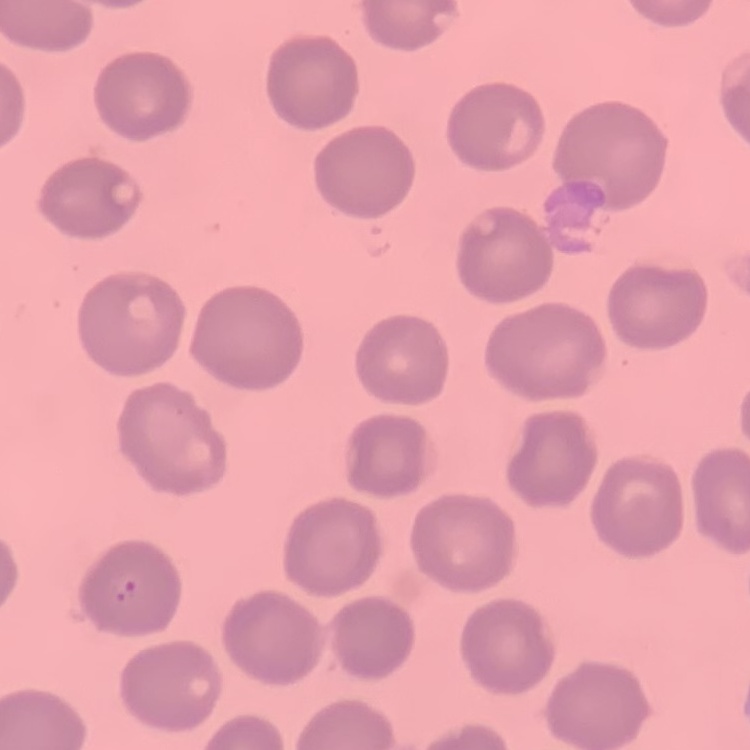
red blood cell morphology = no rouleaux formation
stain = Field's or Giemsa
preparation = thin blood smear
image type = one tile cut from a larger photomicrograph